Classify this cell by malaria status.
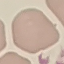
It is uninfected.

preparation = thin smear
stain = Giemsa
image type = cell patch, automatically extracted from a larger field of view and resized to 64 × 64 pixels
capture = smartphone camera at the microscope eyepiece